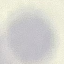 Malaria status: uninfected. Acquired by smartphone through the microscope eyepiece. Automatically extracted cell patch, resized to 64 × 64 pixels. Giemsa-stained preparation. Thin blood film.